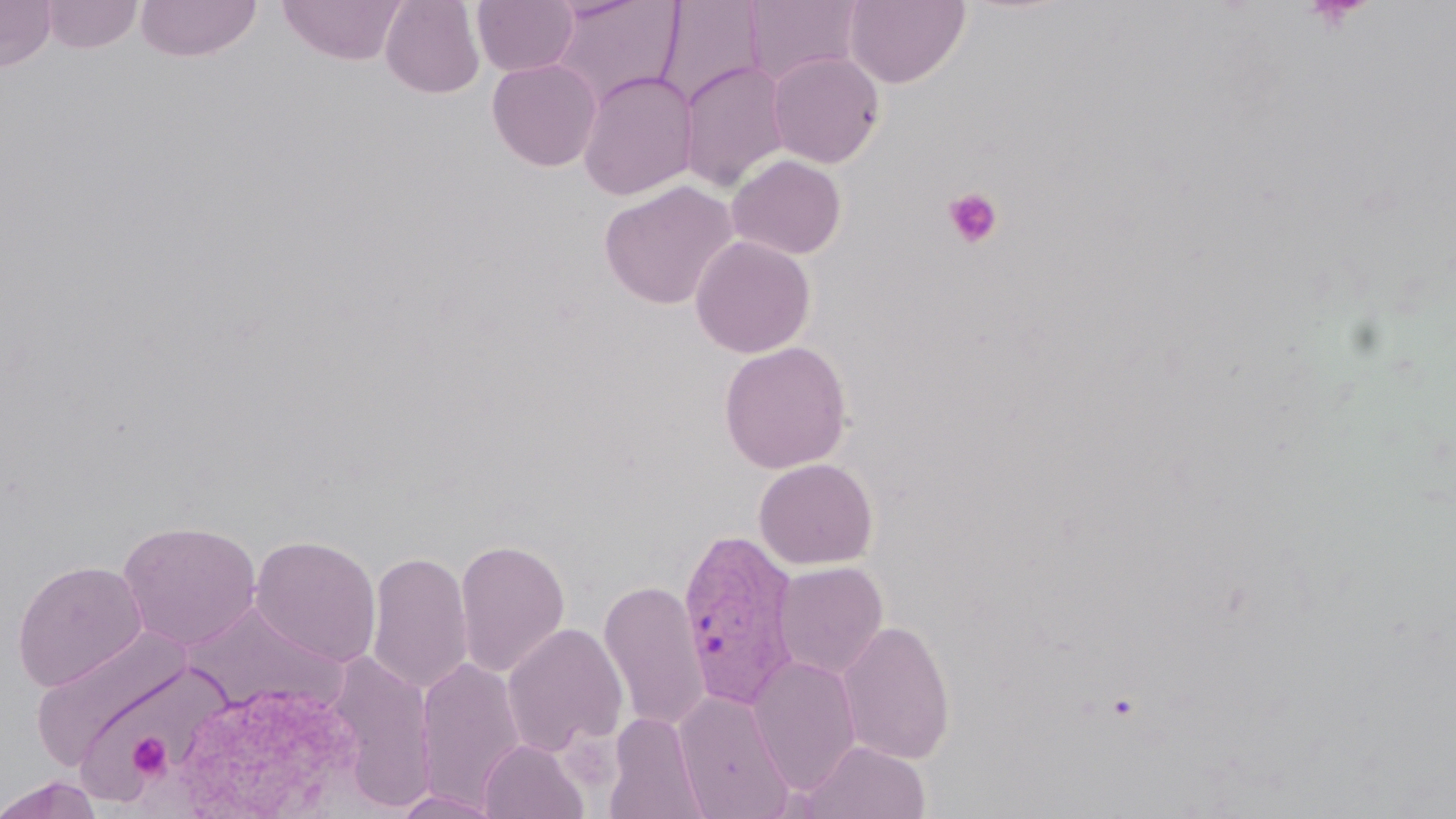 Approximate bounding boxes as [x1, y1, x2, y2] in pixels. Plasmodium vivax-infected red blood cell locations: [677, 527, 802, 709]. Uninfected red blood cell locations: [0, 0, 57, 72], [41, 0, 143, 54], [136, 0, 262, 63], [380, 0, 485, 99], [472, 0, 579, 76], [655, 0, 766, 110], [844, 0, 971, 88], [278, 1, 408, 66], [547, 1, 684, 110], [742, 1, 865, 87], [766, 51, 885, 169], [487, 58, 603, 172], [678, 59, 792, 193], [576, 70, 698, 201], [726, 154, 847, 260], [599, 180, 738, 310], [690, 234, 815, 358], [718, 341, 853, 474], [754, 458, 878, 570], [117, 519, 262, 651], [250, 534, 382, 668], [454, 538, 571, 678], [366, 550, 473, 697], [12, 559, 148, 691], [773, 561, 889, 680], [598, 580, 710, 731], [180, 601, 347, 715], [837, 619, 956, 765], [502, 622, 628, 757], [29, 626, 195, 774], [325, 651, 439, 813], [748, 655, 861, 795], [414, 656, 528, 812], [167, 680, 368, 818], [674, 689, 795, 818], [604, 712, 707, 819], [478, 739, 588, 819], [801, 739, 931, 819], [0, 775, 105, 819], [390, 789, 507, 818]. Platelet locations: [943, 187, 1004, 249], [127, 732, 171, 780]. Slide-level diagnosis: Plasmodium vivax. Captured at 1000x magnification. Thin blood smear. Image is 1456×819 pixels. May-Grünwald-Giemsa-stained preparation. Optical microscopy. Single field of view.